Classify this cell by malaria status.
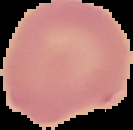
It is uninfected.

Summary:
  - Image size: 133×130 pixels
  - Image type: segmented cell region with the area outside set to black
  - Preparation: thin blood film